Assess this cell for malaria.
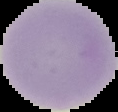

It is uninfected.

Image is 118×112 pixels. Cell region segmented out of the field of view; the surrounding area is masked to black. From a thin blood film.